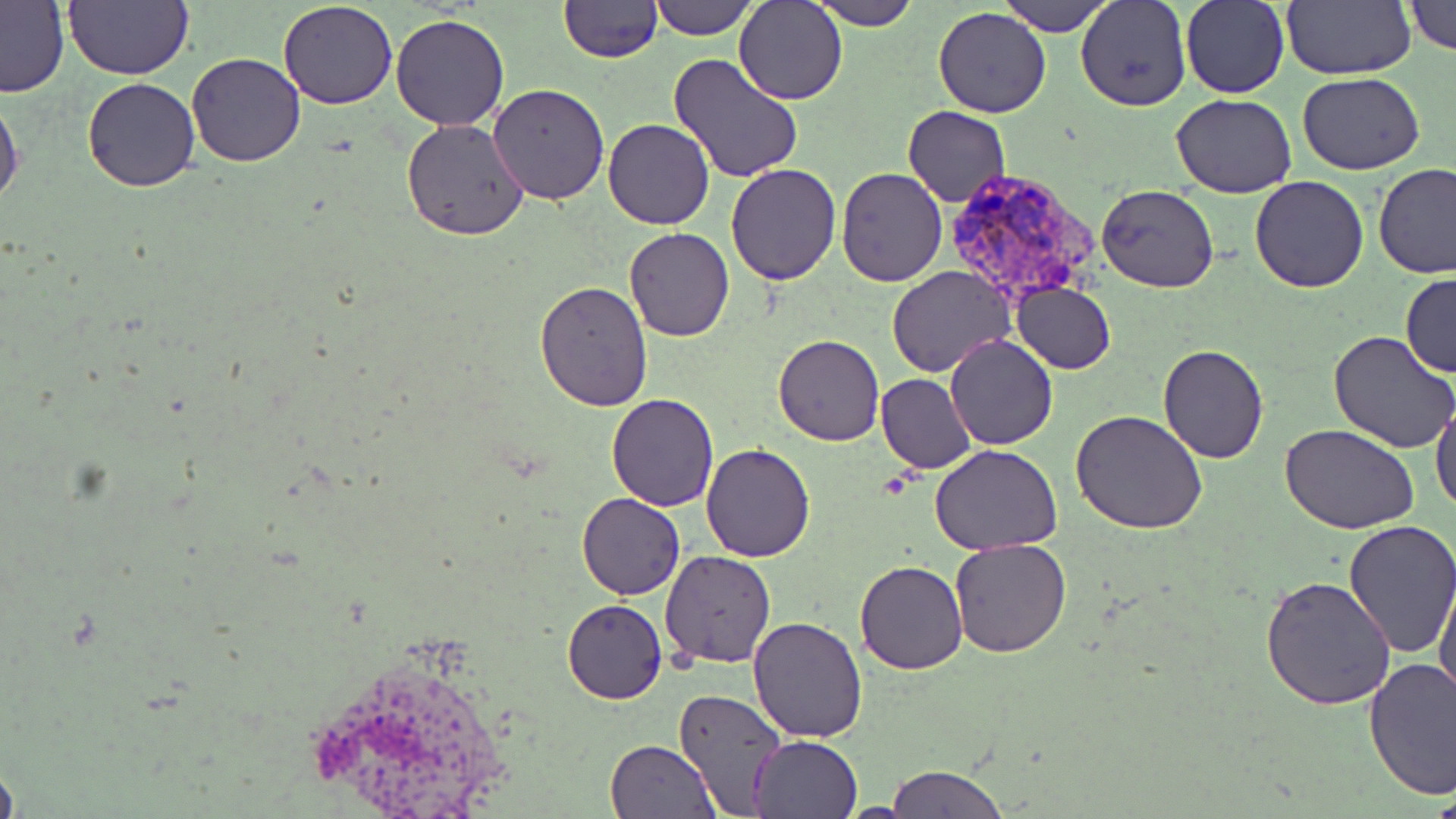
{
  "slide_level_diagnosis": "Plasmodium vivax",
  "modality": "optical microscopy",
  "image_size": "1456×819 pixels",
  "stain": "May-Grünwald-Giemsa",
  "preparation": "thin blood smear",
  "magnification": "1000x",
  "plasmodium_vivax_infected_red_blood_cell_locations": "approximate bounding boxes as [x1, y1, x2, y2] in pixels: [940, 166, 1100, 307]",
  "uninfected_red_blood_cell_locations": "approximate bounding boxes as [x1, y1, x2, y2] in pixels: [64, 0, 193, 80], [648, 0, 756, 39], [734, 0, 848, 106], [808, 0, 920, 30], [1000, 0, 1114, 36], [1076, 0, 1191, 111], [1179, 0, 1289, 99], [1281, 0, 1415, 81], [0, 1, 69, 97], [277, 1, 398, 110], [558, 1, 663, 64], [1401, 1, 1456, 54], [933, 6, 1051, 118], [391, 15, 509, 132], [187, 51, 305, 166], [666, 52, 807, 185], [1297, 72, 1424, 175], [81, 75, 201, 192], [488, 83, 611, 203], [0, 91, 24, 213], [1170, 93, 1296, 198], [904, 105, 1010, 207], [401, 118, 530, 240], [603, 118, 714, 230], [724, 163, 841, 286], [1372, 163, 1456, 277], [836, 167, 947, 286], [1249, 175, 1370, 292], [1096, 184, 1219, 292], [623, 227, 734, 342], [885, 266, 1015, 378], [1400, 273, 1455, 378], [537, 280, 652, 410], [1011, 282, 1116, 374], [1330, 330, 1456, 452], [773, 332, 885, 447], [945, 334, 1057, 451], [1156, 344, 1269, 464], [876, 374, 977, 473], [606, 394, 719, 511], [1431, 398, 1456, 517], [1070, 411, 1207, 535], [1282, 423, 1422, 535], [701, 444, 815, 562], [930, 444, 1061, 555], [578, 493, 685, 601], [1342, 520, 1456, 657], [948, 539, 1072, 658], [660, 550, 777, 668], [856, 560, 969, 675], [1261, 573, 1396, 709], [1434, 574, 1456, 709], [563, 600, 667, 704], [749, 615, 867, 740], [1363, 656, 1456, 801], [673, 687, 789, 817], [751, 735, 862, 819], [604, 738, 718, 819], [885, 765, 1009, 818]",
  "field_of_view": "one of a larger specimen"
}